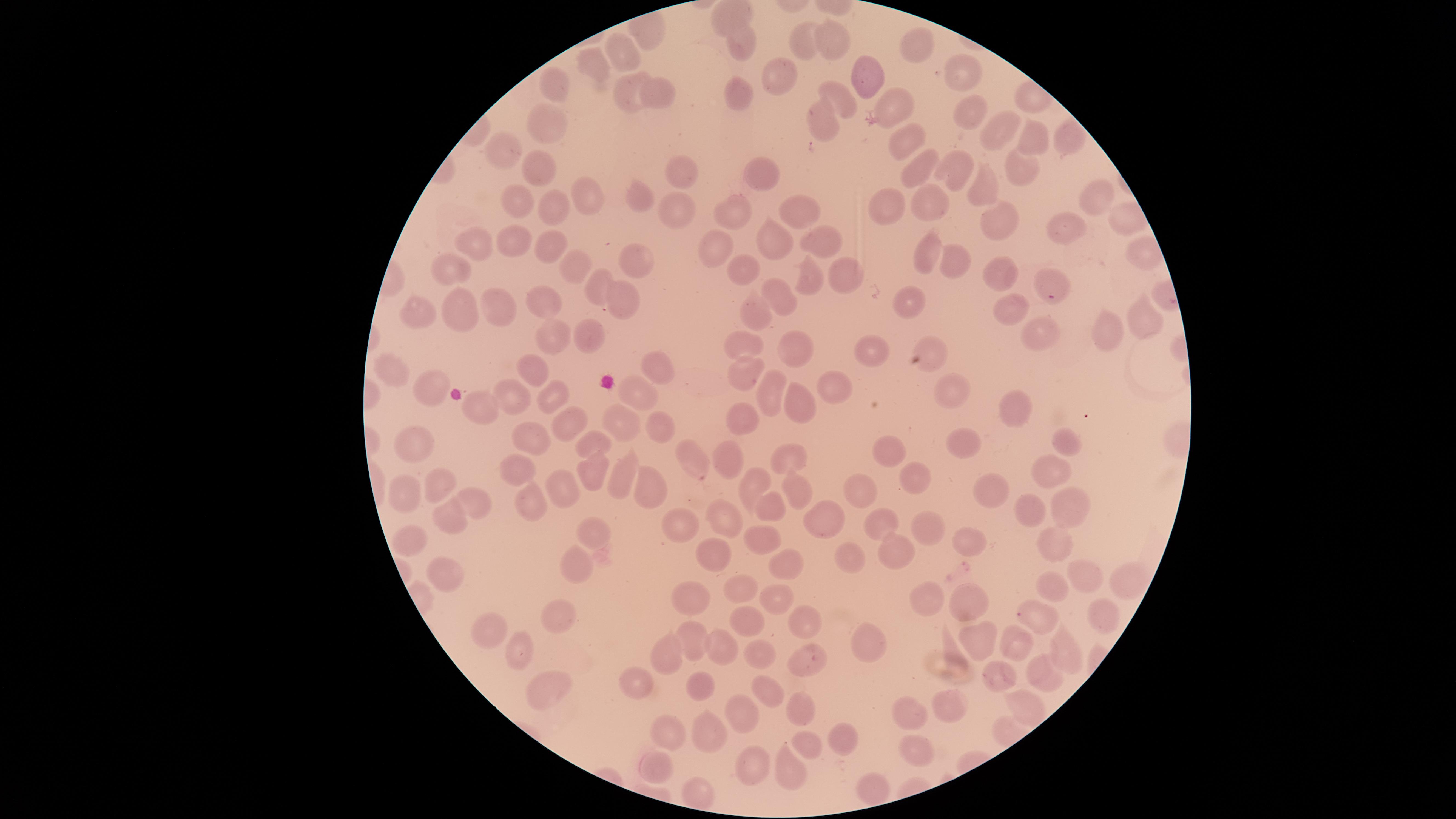
Approximate marker points as [x, y] in pixels.
Summary:
  - Uninfected RBCs: [808, 36], [836, 40], [749, 44], [917, 47], [623, 51], [598, 57], [964, 72], [871, 75], [777, 76], [555, 85], [630, 90], [665, 90], [736, 93], [840, 101], [890, 106], [968, 112], [820, 124], [999, 127], [1069, 130], [548, 131], [903, 139], [1032, 139], [507, 146], [951, 166], [1019, 168], [538, 170], [911, 173], [761, 176], [677, 177], [973, 183], [589, 193], [638, 193], [517, 198], [928, 198], [1098, 202], [673, 205], [737, 206], [890, 206], [548, 209], [799, 215], [1003, 217], [1063, 227], [821, 236], [770, 237], [511, 239], [471, 242], [552, 243], [925, 251], [716, 252], [635, 257], [571, 262], [952, 264], [454, 265], [841, 269], [740, 271], [996, 272], [813, 273], [1049, 282], [598, 287], [622, 294], [782, 297], [545, 301], [907, 302], [461, 307], [1007, 308], [499, 309], [419, 311], [755, 313], [1140, 321], [1039, 331], [1109, 332], [548, 334], [594, 336], [746, 344], [798, 345], [930, 352], [882, 353], [394, 366], [536, 368], [655, 369], [745, 370], [431, 382], [833, 389], [771, 390], [556, 391], [950, 394], [638, 396], [801, 400], [515, 402], [1004, 405], [481, 411], [748, 413], [564, 421], [658, 423], [613, 427], [1071, 435], [537, 437], [594, 439], [420, 440], [968, 444], [894, 451], [793, 454], [693, 455], [728, 461], [508, 465], [1049, 466], [593, 473], [623, 473], [917, 477], [759, 486], [435, 489], [565, 489], [995, 490], [652, 491], [861, 493], [401, 495], [799, 496], [536, 498], [1065, 506], [473, 510], [769, 510], [1036, 513], [727, 515], [448, 518], [885, 519], [823, 520], [921, 521], [685, 522], [590, 530], [411, 536], [760, 544], [969, 544], [714, 548], [1051, 548], [893, 549], [841, 553], [785, 556], [445, 566], [571, 566], [1080, 577], [1119, 584], [1054, 586], [744, 588], [692, 591], [778, 598], [927, 598], [976, 598], [560, 611], [1039, 611], [1100, 615], [805, 619], [749, 622], [986, 632], [694, 633], [489, 634], [873, 644], [1012, 644], [1064, 646], [669, 648], [719, 648], [518, 652], [755, 656], [811, 659], [1044, 671], [998, 675], [639, 680], [772, 685], [544, 686], [703, 687], [1024, 703], [744, 707], [951, 707], [801, 711], [907, 718], [668, 724], [710, 732], [841, 736], [806, 740], [914, 751], [662, 761], [749, 765], [789, 768], [874, 784], [698, 798]
  - Capture: smartphone photograph through the microscope eyepiece
  - Stain: Giemsa
  - Field of view: single
  - Presence: no malaria parasites detected
  - Visible region: circular
  - Preparation: thin blood film
  - Image size: 1456×819 pixels